Name the parasite shown.
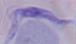
This is a trypanosome.

magnification = 1000x
modality = micrograph